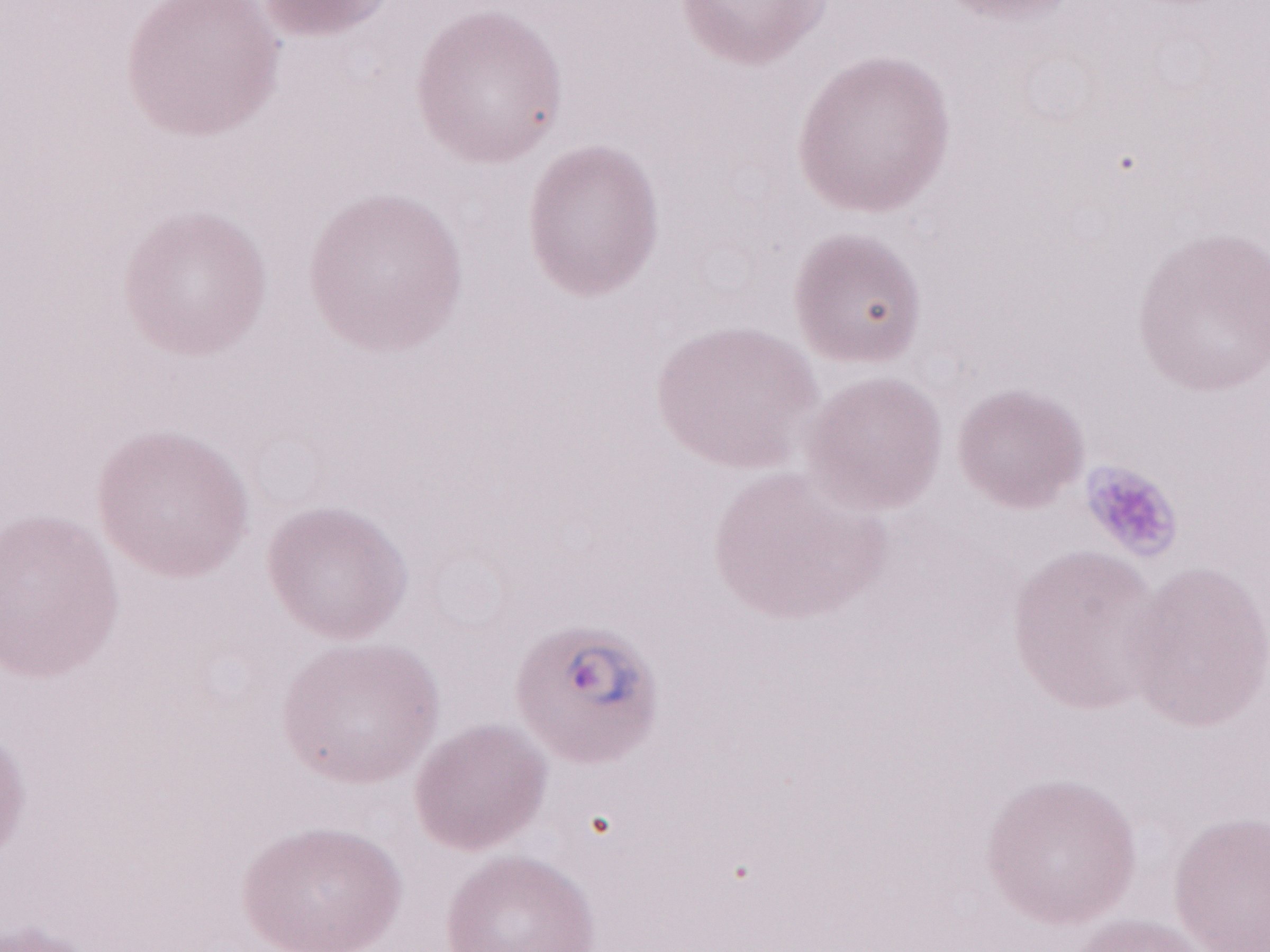 One field of this slide. Image is 1270×952 pixels. Olympus BX43 microscope and DP73 digital camera. 1,000x magnification. Patient diagnosis: malaria infection. May-Grünwald-Giemsa-stained preparation. Thin peripheral-blood smear.